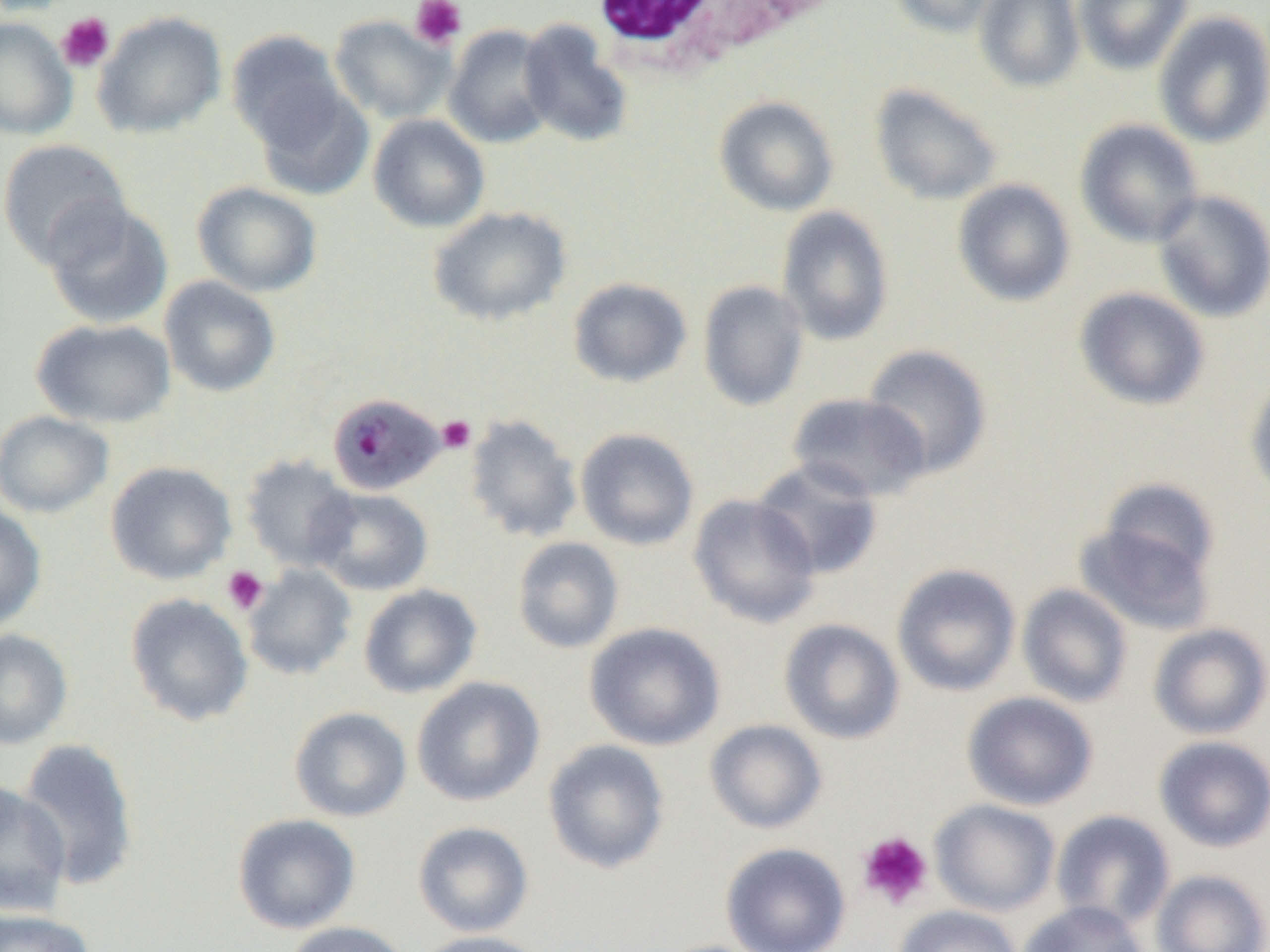

Summary:
  - Coordinate format: approximate bounding boxes as (x1, y1, x2, y2) in pixels
  - White blood cell locations: (582, 0, 846, 76)
  - Plasmodium malariae-infected red blood cell locations: (327, 392, 445, 495)
  - Platelet locations: (410, 0, 467, 49), (56, 12, 115, 73), (437, 415, 476, 454), (222, 565, 269, 615), (856, 831, 934, 910)
  - Uninfected red blood cell locations: (0, 0, 80, 16), (888, 0, 1005, 37), (974, 0, 1084, 92), (1073, 0, 1194, 75), (92, 11, 227, 139), (1153, 11, 1270, 148), (329, 14, 454, 124), (0, 17, 78, 140), (518, 20, 633, 148), (443, 24, 558, 148), (225, 29, 348, 149), (250, 81, 375, 202), (869, 83, 1003, 206), (714, 95, 839, 216), (368, 113, 490, 233), (1074, 119, 1204, 248), (0, 138, 131, 268), (952, 179, 1077, 307), (192, 181, 323, 298), (1152, 190, 1270, 323), (40, 199, 174, 329), (776, 205, 894, 346), (428, 206, 571, 326), (159, 275, 281, 397), (567, 277, 693, 388), (697, 279, 809, 412), (1074, 287, 1210, 411), (31, 318, 177, 428), (861, 344, 993, 480), (1245, 376, 1270, 503), (787, 392, 932, 503), (0, 410, 114, 518), (463, 413, 583, 544), (575, 428, 699, 551), (240, 454, 359, 572), (751, 458, 883, 580), (105, 461, 237, 585), (1099, 478, 1220, 582), (311, 487, 433, 595), (687, 493, 821, 628), (0, 503, 47, 631), (1074, 521, 1216, 635), (512, 536, 625, 654), (892, 563, 1021, 697), (242, 564, 357, 680), (358, 584, 482, 698), (1017, 584, 1133, 708), (124, 592, 254, 726), (779, 618, 905, 744), (584, 622, 726, 751), (1149, 623, 1270, 740), (0, 629, 73, 749), (412, 676, 545, 806), (962, 691, 1098, 811), (289, 706, 412, 822), (704, 719, 827, 834), (1154, 735, 1270, 852), (16, 738, 140, 891), (542, 739, 671, 874), (0, 783, 71, 917), (930, 799, 1060, 917), (1051, 809, 1175, 931), (232, 813, 361, 935), (412, 821, 534, 937), (720, 842, 851, 952), (1151, 869, 1270, 952), (1017, 900, 1150, 952), (893, 905, 1022, 952), (0, 909, 97, 952), (283, 921, 413, 952), (410, 930, 551, 952)
  - Slide-level diagnosis: Plasmodium malariae
  - Image size: 1270×952 pixels
  - Preparation: thin blood smear
  - Field of view: single
  - Magnification: 1000x
  - Modality: light microscopy